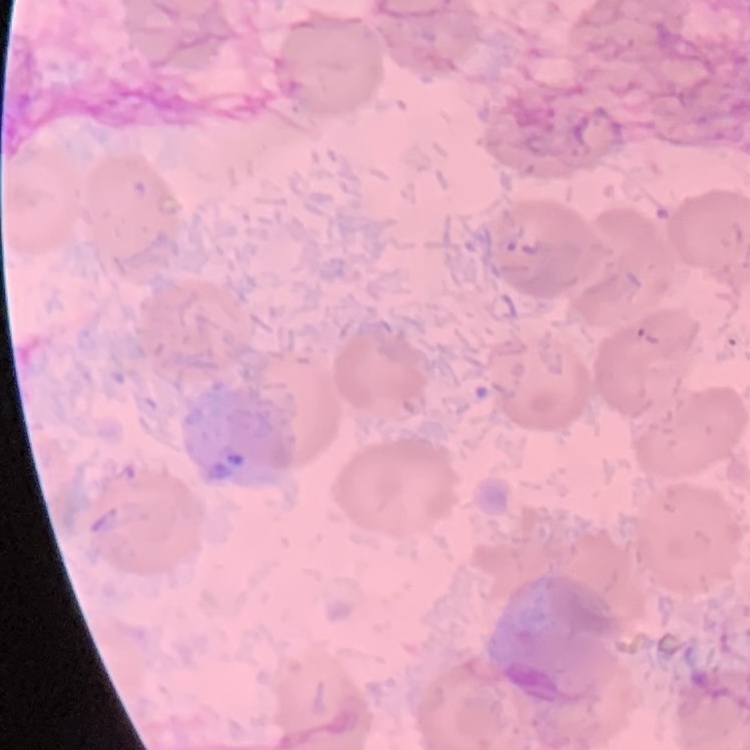 The red blood cells show no rouleaux formation. Square crop of a larger photomicrograph. Thin peripheral smear. Field's or Giemsa stain.